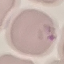
result = no malaria parasites detected
capture = smartphone through the microscope eyepiece
image type = automatically extracted cell patch, resized to 64 × 64 pixels
stain = Giemsa
preparation = thin smear